Classify this cell by malaria status.
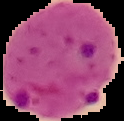

Parasitized.

preparation = thin blood film
image size = 124×121 pixels
image type = segmented cell region on a black background